Locate every Plasmodium parasite by life-cycle stage, and every leukocyte.
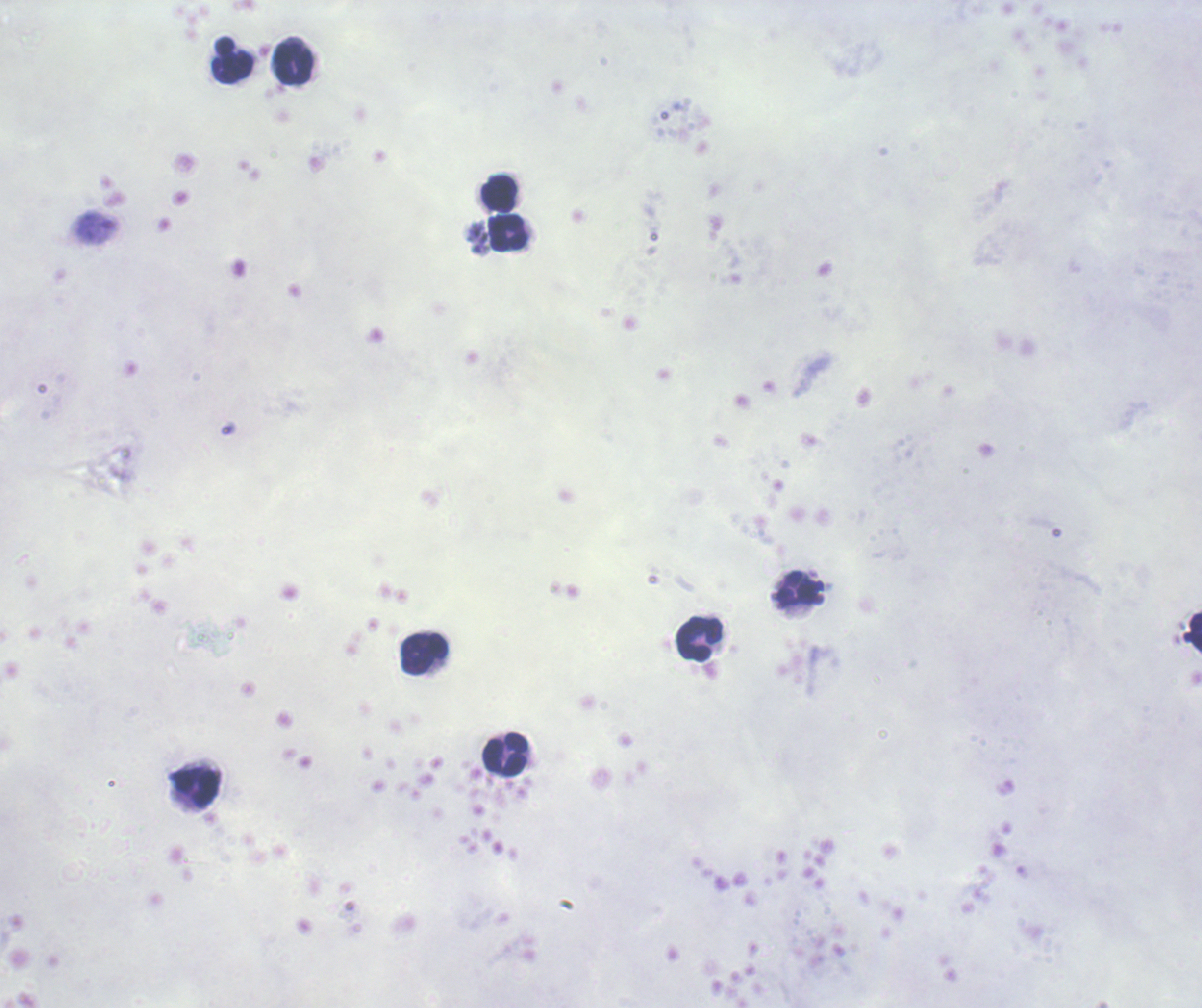
No Plasmodium parasites seen.
Approximate centers as [x, y] in pixels.
Leukocytes: [233, 59], [293, 60], [499, 195], [508, 233], [1195, 632], [699, 639], [424, 653], [504, 754], [195, 786].

{
  "image_size": "1202×1008 pixels",
  "background_quality": "poor",
  "magnification": "100x",
  "context": "previously used in a real diagnosis",
  "preparation": "thick blood film",
  "stain": "Romanowsky",
  "field_of_view": "one from this slide"
}